Give the position of every Plasmodium parasite.
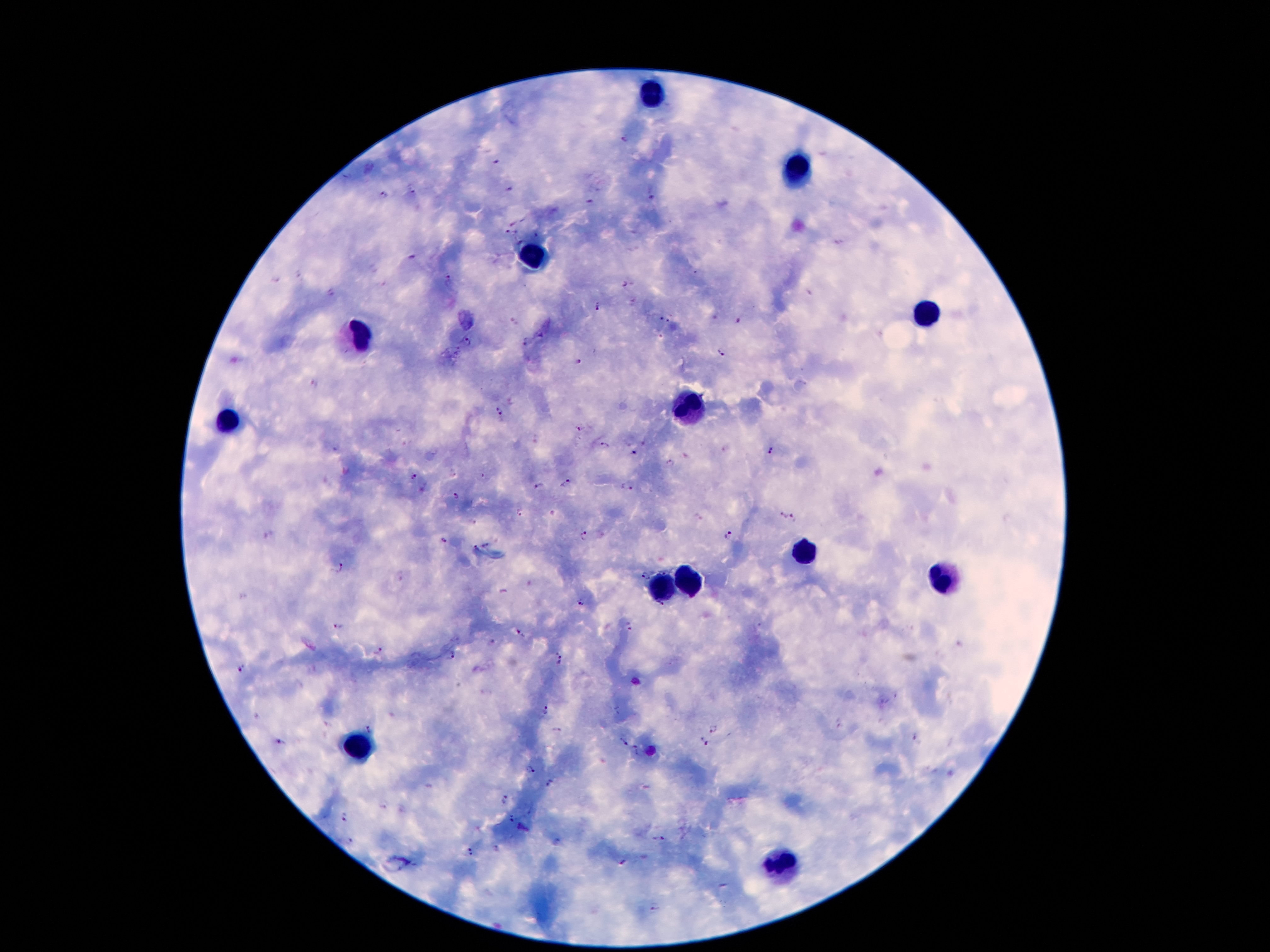

Approximate centers as [x, y] in pixels.
Plasmodium parasites: [625, 140], [496, 160], [508, 187], [412, 189], [384, 195], [652, 195], [591, 202], [506, 232], [520, 243], [414, 255], [298, 275], [449, 278], [624, 286], [330, 294], [597, 307], [663, 319], [737, 320], [526, 342], [467, 343], [722, 352], [578, 363], [500, 411], [577, 429], [603, 446], [770, 452], [633, 455], [671, 463], [412, 476], [566, 484], [539, 487], [626, 487], [456, 498], [519, 513], [795, 516], [781, 517], [583, 536], [729, 537], [442, 540], [488, 545], [474, 549], [338, 566], [642, 577], [582, 601], [660, 604], [339, 626], [629, 627], [522, 634], [493, 642], [378, 652], [451, 656], [560, 662], [241, 668], [545, 710], [838, 723], [369, 727], [713, 728], [915, 738], [280, 741], [624, 742], [704, 742], [635, 750], [530, 770], [549, 783], [505, 800], [383, 804], [343, 815], [512, 819], [659, 839], [350, 841], [495, 849], [471, 853], [622, 863], [654, 906].

Summary:
  - Leukocyte locations: [650, 95], [796, 171], [529, 255], [927, 312], [358, 332], [687, 411], [225, 421], [803, 554], [690, 581], [942, 581], [660, 586], [353, 747], [779, 863]
  - Patient malaria status: infected with Plasmodium falciparum
  - Image size: 1270×952 pixels
  - Field of view: single
  - Preparation: thick peripheral-blood smear
  - Capture: smartphone camera through the microscope eyepiece
  - Magnification: 100x
  - Stain: Giemsa